Identify the parasite.
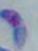
This is Toxoplasma gondii.

Captured at 1000x magnification. Photomicrograph.